Assess the morphology of the red blood cells.
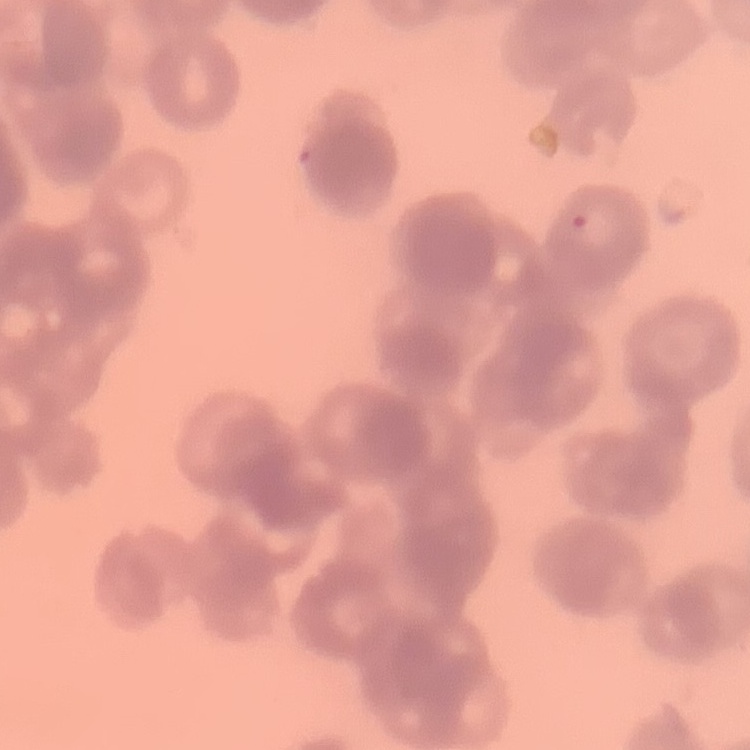
Rouleaux formation.

Square crop of a larger photomicrograph. Thin peripheral smear. Field's or Giemsa stain.